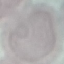
{
  "malaria_status": "uninfected",
  "image_type": "automatically extracted cell patch, resized to 64 × 64 pixels",
  "stain": "Giemsa",
  "preparation": "thin blood smear",
  "capture": "smartphone camera at the microscope eyepiece"
}